Assess this cell for malaria.
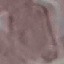

Uninfected.

{
  "image_type": "automatically extracted cell patch, resized to 64 × 64 pixels",
  "capture": "smartphone camera at the microscope eyepiece",
  "stain": "Giemsa",
  "preparation": "thin blood smear"
}